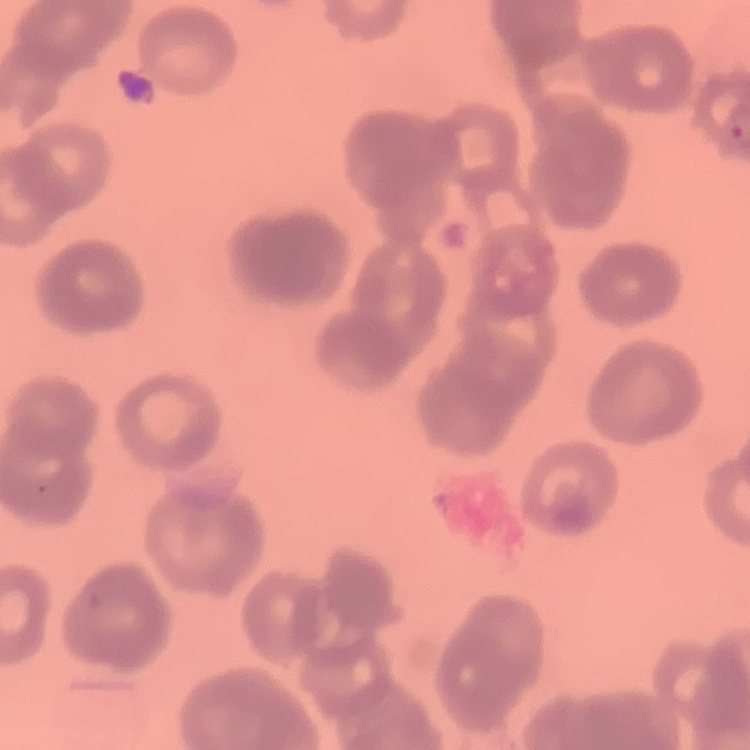
red_blood_cell_morphology: rouleaux formation
stain: Field's or Giemsa
image_type: one tile cut from a larger photomicrograph
preparation: thin blood smear